Classify this cell by malaria status.
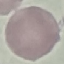

It is uninfected.

capture = smartphone through the microscope eyepiece
image type = automatically extracted cell patch, resized to 64 × 64 pixels
stain = Giemsa
preparation = thin smear